Identify the parasite.
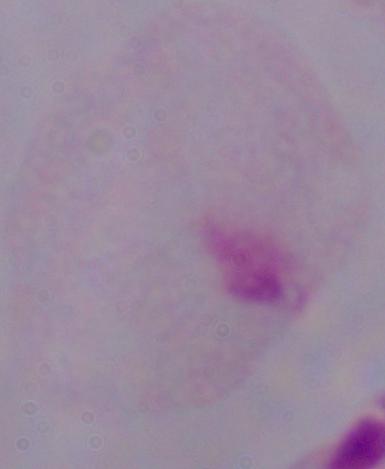
This is a trichomonad.

{
  "magnification": "1000x",
  "modality": "photomicrograph"
}